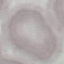
result = no malaria parasites detected
preparation = thin blood smear
capture = smartphone camera at the microscope eyepiece
stain = Giemsa
image type = cell patch, automatically extracted from a larger field of view and resized to 64 × 64 pixels